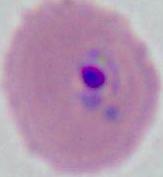

identification: Plasmodium
modality: micrograph
magnification: 400x or 1000x